Classify the preparation.
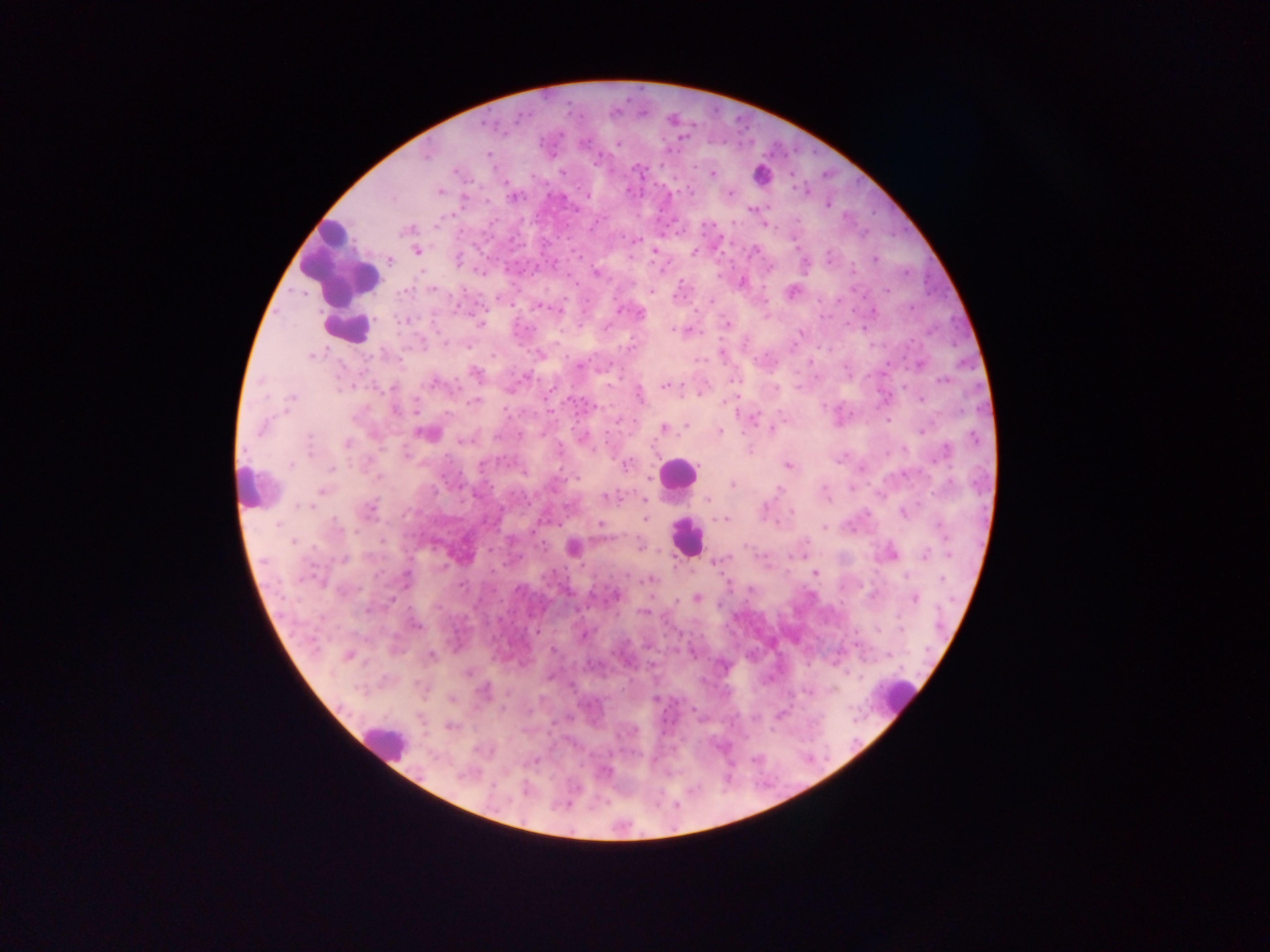

Thick blood film.

Approximate centers as {x, y} in pixels. Plasmodium parasite locations: {617, 144}, {427, 155}, {487, 155}, {596, 160}, {637, 170}, {562, 172}, {712, 173}, {441, 191}, {729, 193}, {513, 197}, {752, 209}, {406, 231}, {417, 251}, {694, 253}, {458, 260}, {875, 260}, {389, 261}, {853, 269}, {480, 272}, {596, 273}, {742, 282}, {433, 289}, {404, 291}, {888, 291}, {792, 292}, {539, 308}, {911, 308}, {558, 310}, {640, 313}, {403, 320}, {480, 323}, {727, 324}, {608, 326}, {679, 330}, {673, 331}, {800, 333}, {446, 343}, {467, 347}, {630, 347}, {540, 354}, {312, 355}, {579, 366}, {476, 373}, {942, 380}, {434, 383}, {666, 385}, {392, 387}, {640, 395}, {291, 398}, {921, 400}, {474, 402}, {395, 410}, {752, 419}, {686, 425}, {262, 427}, {664, 428}, {772, 429}, {921, 429}, {720, 431}, {423, 433}, {519, 435}, {584, 436}, {973, 437}, {309, 441}, {461, 441}, {347, 443}, {560, 449}, {943, 453}, {291, 465}, {626, 465}, {789, 465}, {332, 468}, {379, 477}, {577, 478}, {732, 484}, {950, 484}, {779, 489}, {321, 492}, {607, 498}, {708, 499}, {645, 501}, {301, 505}, {370, 509}, {765, 509}, {792, 511}, {904, 513}, {645, 518}, {723, 520}, {278, 524}, {335, 524}, {601, 524}, {824, 527}, {942, 528}, {293, 541}, {806, 542}, {640, 545}, {573, 548}, {893, 554}, {925, 555}, {344, 559}, {720, 560}, {814, 573}, {406, 578}, {943, 579}, {651, 580}, {616, 596}, {697, 598}, {915, 598}, {368, 610}, {642, 612}, {416, 625}, {901, 628}, {877, 629}, {537, 631}, {552, 650}, {348, 655}, {432, 655}, {466, 673}, {483, 691}, {452, 698}, {654, 698}, {451, 726}, {535, 761}, {604, 771}, {463, 775}. Leukocyte locations: {769, 170}, {340, 263}, {348, 328}, {677, 473}, {243, 486}, {685, 537}, {898, 697}, {384, 741}. Photographed through a microscope with a mobile-phone camera. Image is 1270×952 pixels. Sample from Ghana. One field of view.